Evaluate for Plasmodium parasites.
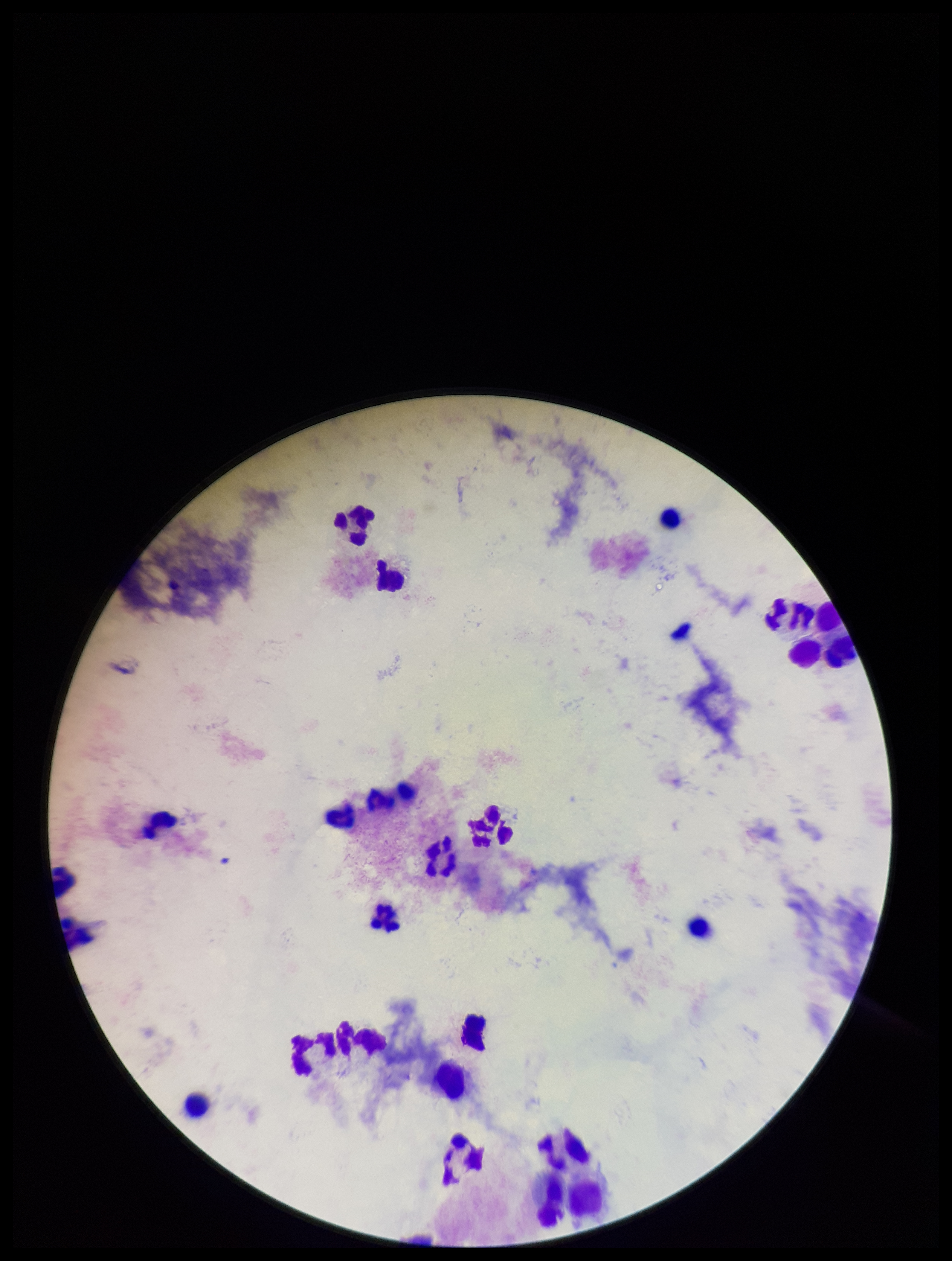

None seen.

{
  "preparation": "thick blood smear",
  "stain": "Giemsa",
  "capture": "smartphone photograph through the microscope eyepiece",
  "leukocyte_count": 26,
  "field_of_view": "single",
  "patient_malaria_status": "negative",
  "image_size": "952×1261 pixels",
  "parasite_count": 0
}